State the blood parasite species.
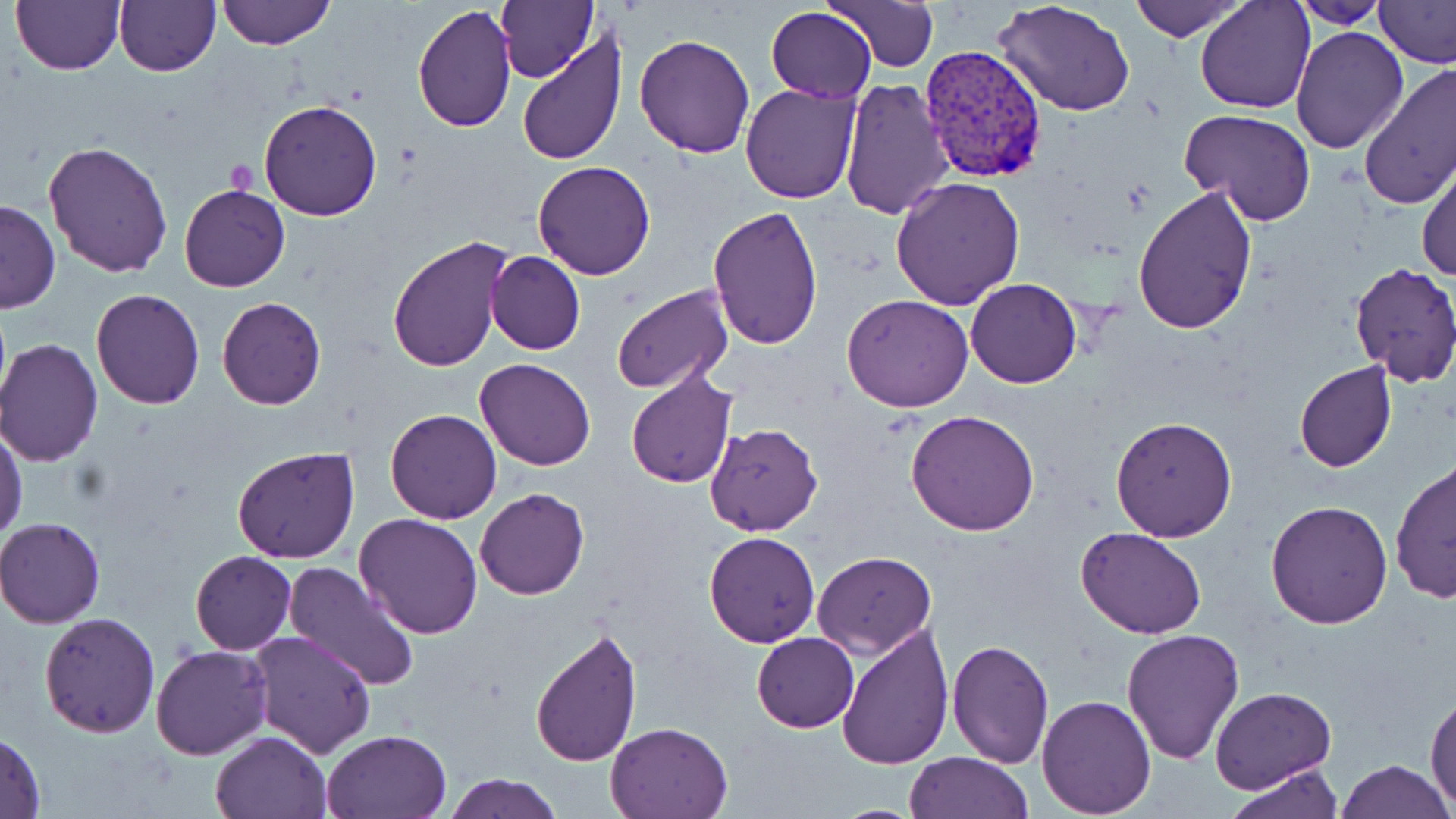
Plasmodium vivax.

Approximate bounding boxes as (x1,y1)-(x2,y2) corner pairs in pixels. Platelet locations: (224,160)-(258,198). Uninfected red blood cell locations: (11,0)-(125,75), (114,0)-(220,75), (216,0)-(334,49), (497,0)-(598,83), (826,0)-(939,72), (1129,0)-(1245,40), (1195,0)-(1315,113), (1288,0)-(1388,29), (1372,0)-(1456,67), (995,1)-(1138,116), (411,6)-(518,133), (766,7)-(877,103), (1290,25)-(1409,154), (515,32)-(629,166), (634,32)-(755,158), (1357,62)-(1456,210), (838,79)-(954,220), (741,82)-(860,204), (260,100)-(382,220), (1178,108)-(1316,225), (44,141)-(173,277), (1417,155)-(1456,283), (533,160)-(655,280), (891,175)-(1024,310), (178,183)-(290,293), (1132,184)-(1257,333), (0,198)-(60,315), (707,205)-(823,350), (387,236)-(512,373), (486,250)-(585,356), (1349,263)-(1456,387), (966,279)-(1081,387), (611,284)-(735,393), (92,288)-(205,409), (841,293)-(973,411), (216,296)-(326,410), (0,340)-(103,466), (475,358)-(596,471), (1293,361)-(1397,472), (625,369)-(738,489), (386,409)-(501,524), (905,409)-(1041,536), (1111,415)-(1237,540), (705,423)-(823,536), (0,426)-(27,543), (232,446)-(360,565), (1390,459)-(1456,603), (475,488)-(589,600), (1266,499)-(1394,629), (355,514)-(484,640), (0,517)-(106,628), (1078,527)-(1205,640), (702,531)-(820,647), (189,550)-(296,655), (812,551)-(936,657), (283,561)-(421,692), (39,611)-(162,737), (531,621)-(642,765), (835,621)-(954,771), (1122,628)-(1246,764), (249,629)-(377,758), (752,632)-(859,732), (947,640)-(1053,767), (150,644)-(272,760), (1210,685)-(1337,794), (1426,691)-(1456,806), (1037,695)-(1156,818), (606,720)-(733,818), (0,729)-(45,817), (321,729)-(450,818), (211,731)-(330,819), (903,752)-(1035,819), (1335,759)-(1453,819), (1226,765)-(1344,819), (444,772)-(560,819). Plasmodium vivax-infected red blood cell locations: (919,45)-(1049,184). Captured at 1000x magnification. One field of a larger specimen. Image is 1456×819 pixels. May-Grünwald-Giemsa-stained preparation. Thin blood film. Light microscopy.